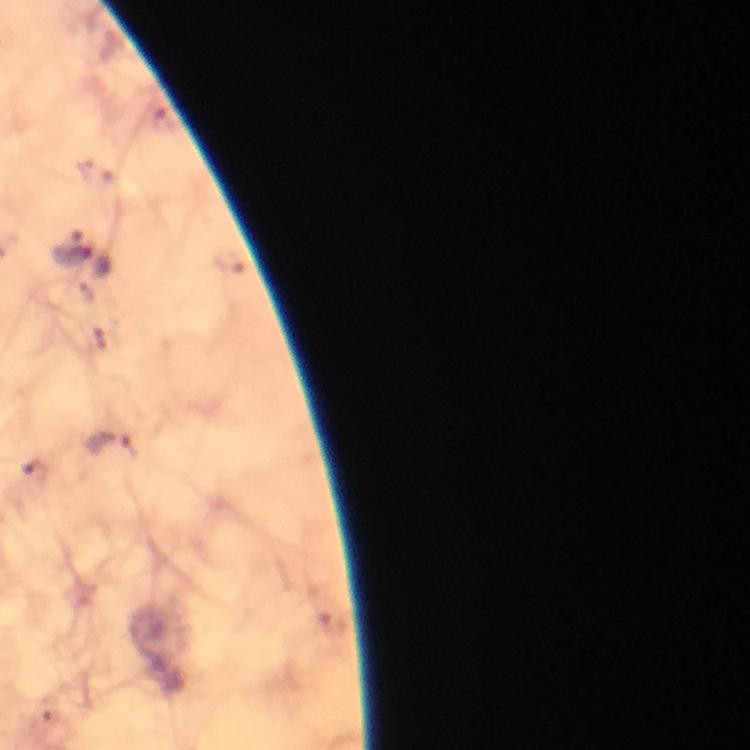

{
  "context": "from a malaria diagnostic workup",
  "malaria_parasite_locations": "approximate object centers, in pixels from the top-left corner: (x=73, y=254), (x=113, y=450)",
  "cropped_from": "one field of view",
  "immersion_oil": "used",
  "stain": "Giemsa",
  "magnification": "100x",
  "preparation": "thick blood smear",
  "image_size": "750×750 pixels",
  "capture": "smartphone mounted on the microscope"
}